Report the malaria status of this cell.
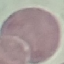
Uninfected.

Summary:
  - Stain: Giemsa
  - Capture: smartphone through the microscope eyepiece
  - Image type: cell patch, automatically extracted from a larger field of view and resized to 64 × 64 pixels
  - Preparation: thin blood smear